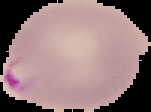 Image is 151×112 pixels. The area outside the segmented cell region is set to black. From a thin blood smear. Result: Plasmodium parasites identified.